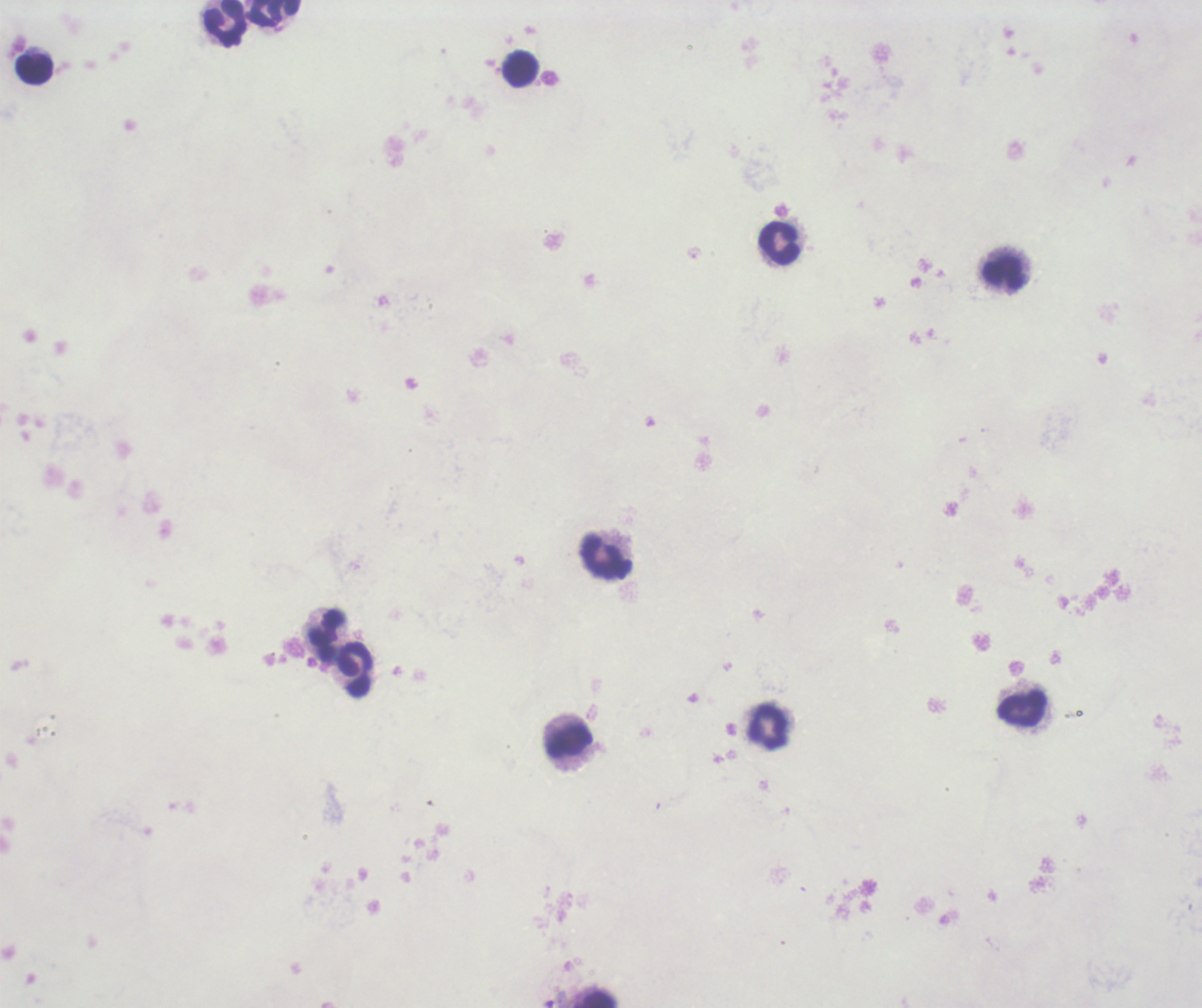
Approximate centers as (x, y) in pixels. Leukocyte locations: (274, 13), (225, 24), (36, 69), (519, 69), (780, 245), (1002, 273), (607, 559), (325, 634), (355, 670), (1021, 707), (769, 727), (569, 742), (601, 1000). Coloration quality: bad. Captured at 100x magnification. Result: no malaria parasites seen. Romanowsky stain. Image is 1202×1008 pixels. Thick blood smear. Background quality: poor. Previously used in an actual diagnosis. One field from this slide.